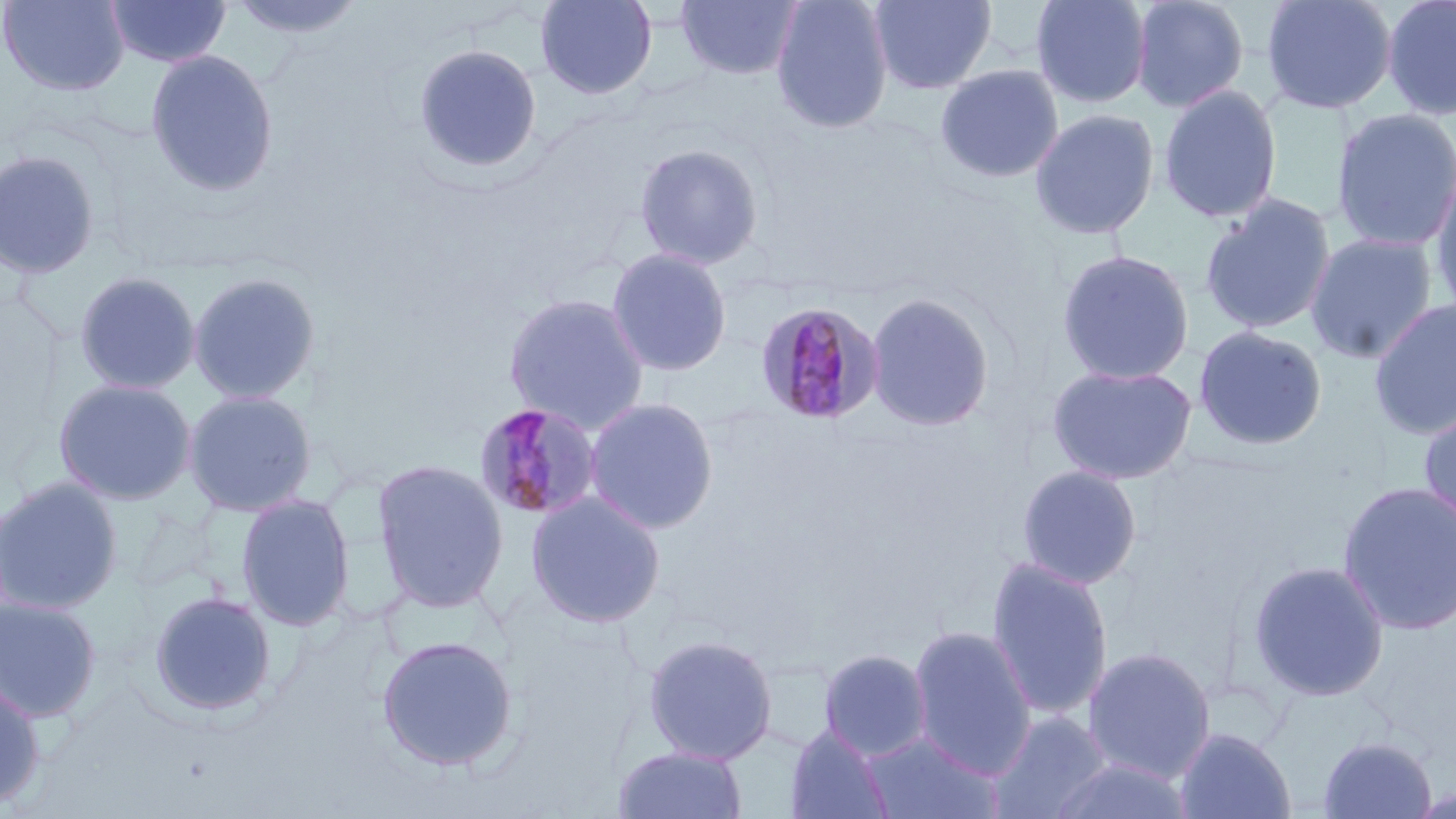

Summary:
  - Coordinate format: approximate bounding boxes as [x1, y1, x2, y2] in pixels
  - Uninfected red blood cell locations: [0, 0, 130, 96], [105, 0, 232, 68], [225, 0, 370, 43], [536, 0, 656, 99], [676, 0, 802, 80], [771, 0, 892, 134], [869, 0, 996, 95], [1030, 0, 1152, 109], [1130, 0, 1250, 113], [1260, 0, 1398, 115], [1382, 0, 1456, 121], [414, 43, 542, 175], [145, 48, 280, 196], [935, 64, 1064, 183], [1158, 84, 1282, 224], [1330, 108, 1456, 253], [1029, 109, 1160, 240], [635, 143, 763, 269], [0, 149, 102, 279], [1430, 166, 1456, 321], [1199, 194, 1337, 335], [1305, 233, 1438, 365], [606, 248, 732, 376], [1056, 249, 1195, 386], [74, 271, 201, 394], [187, 271, 322, 404], [865, 292, 994, 431], [504, 293, 650, 433], [1368, 298, 1456, 441], [1193, 326, 1327, 451], [1047, 363, 1198, 485], [53, 379, 197, 505], [183, 389, 318, 516], [584, 397, 719, 534], [1418, 405, 1456, 534], [371, 459, 509, 612], [1017, 465, 1142, 589], [0, 475, 124, 615], [1337, 480, 1456, 636], [525, 490, 666, 629], [236, 494, 355, 630], [986, 557, 1114, 722], [1247, 559, 1390, 703], [148, 590, 277, 717], [0, 595, 103, 722], [907, 626, 1036, 778], [376, 634, 519, 771], [642, 634, 778, 764], [1082, 646, 1216, 784], [819, 649, 932, 761], [0, 676, 46, 810], [987, 710, 1114, 818], [785, 724, 894, 819], [1174, 726, 1296, 819], [859, 731, 1004, 818], [1317, 735, 1438, 818], [611, 745, 748, 819], [1046, 756, 1194, 818]
  - Plasmodium malariae-infected red blood cell locations: [755, 301, 885, 426], [474, 402, 602, 521]
  - Slide-level diagnosis: Plasmodium malariae
  - Modality: optical microscopy
  - Image size: 1456×819 pixels
  - Magnification: 1000x
  - Field of view: single
  - Preparation: thin blood smear
  - Stain: May-Grünwald-Giemsa